Assess for malaria.
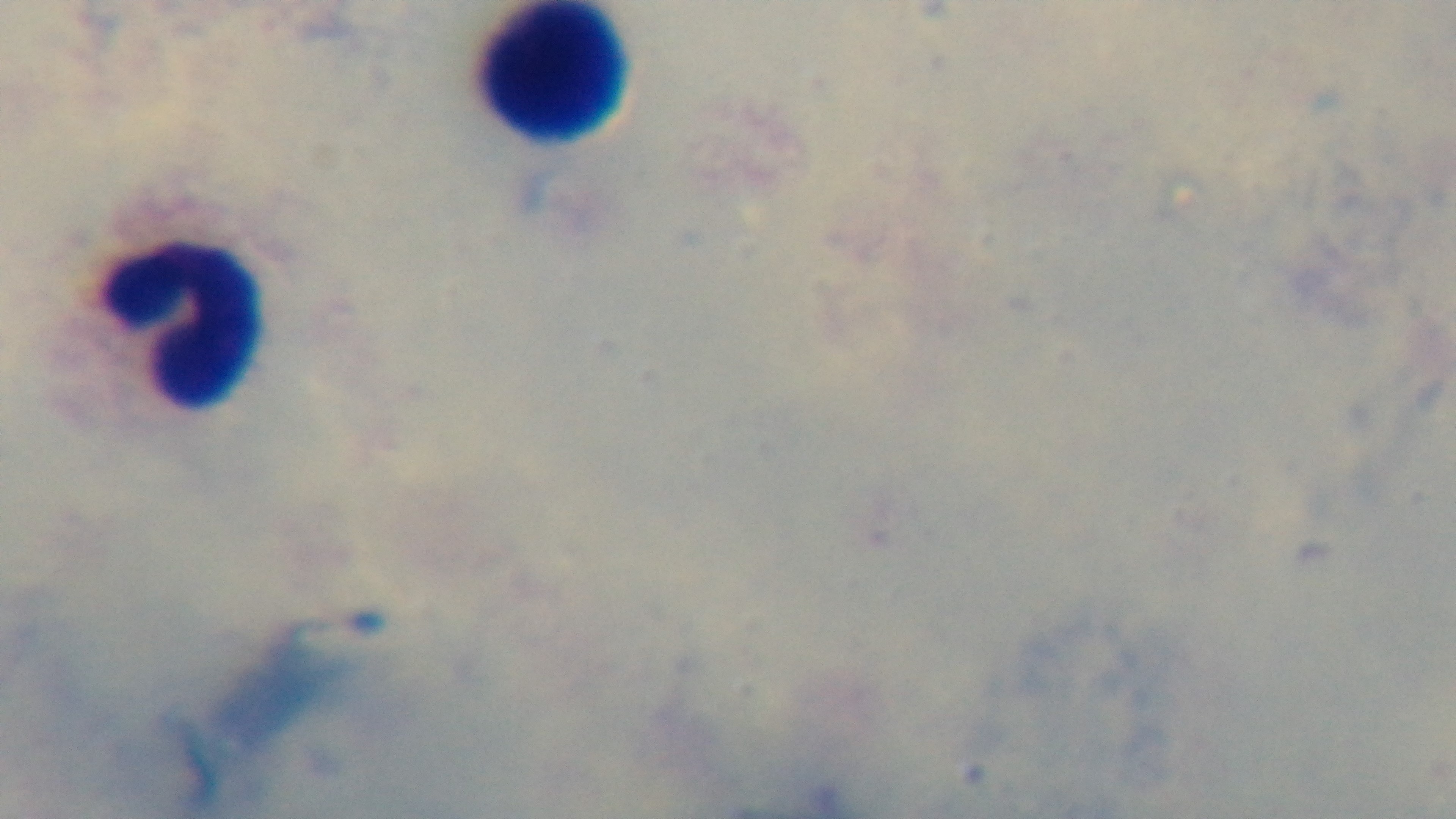
It is uninfected.

Preparation: thick blood film. Giemsa-stained. 100x oil-immersion objective. One field from the slide. Light microscopy. Mounted 4K digital camera.